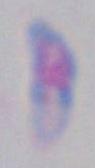

identification = Toxoplasma gondii
magnification = 1000x
modality = micrograph